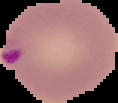 From a thin blood smear. Segmented cell region on a black background. Image is 118×103 pixels. Malaria status: parasitized.